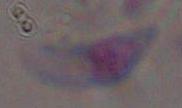
Photomicrograph. 1000x magnification. Toxoplasma gondii is shown.